Identify the parasite.
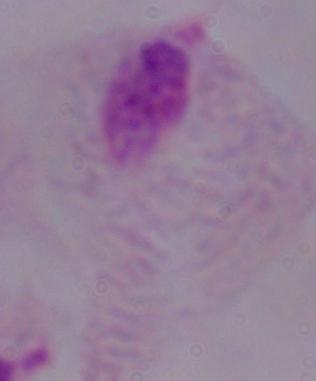
A trichomonad.

Summary:
  - Magnification: 1000x
  - Modality: photomicrograph